Assess this cell for malaria.
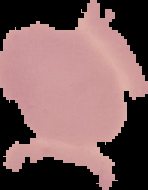

Uninfected.

image type = segmented cell region with the area outside set to black
image size = 148×190 pixels
preparation = thin blood smear